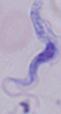
modality = micrograph
magnification = 1000x
identification = trypanosome